Assess this cell for malaria.
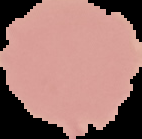

It is uninfected.

Summary:
  - Image size: 142×139 pixels
  - Image type: segmented cell region with the area outside set to black
  - Preparation: thin blood smear